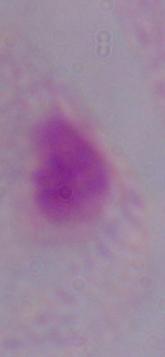 A trichomonad is seen. Photomicrograph. 1000x magnification.